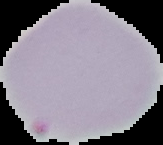
Image is 163×145 pixels. From a thin blood film. Malaria status: parasitized. Cell region segmented out of the field of view; the surrounding area is masked to black.